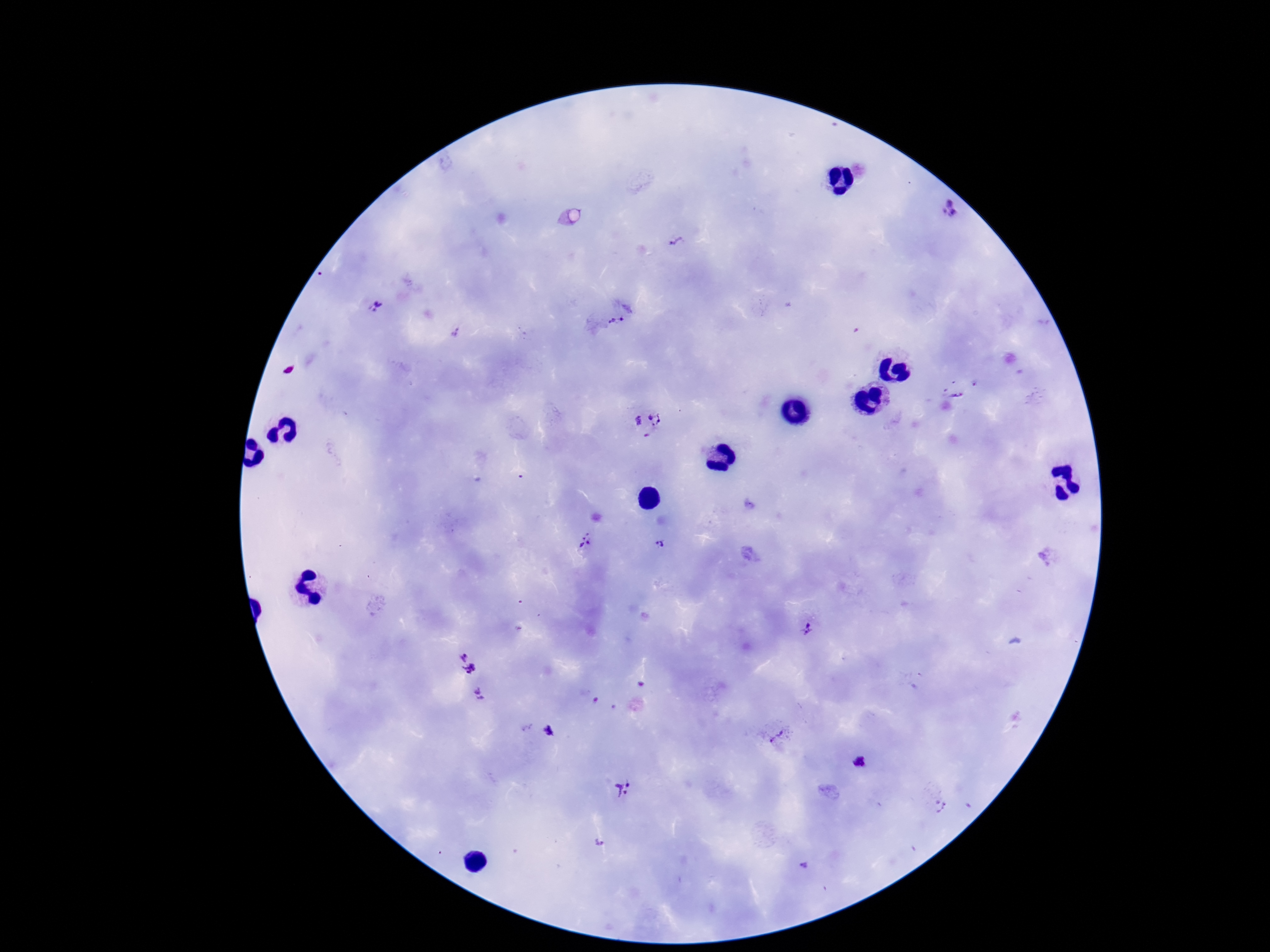
Approximate centers as (x, y) in pixels. Plasmodium parasite locations: (950, 208), (675, 240), (377, 307), (618, 324), (956, 386), (647, 424), (587, 543), (658, 544), (809, 631), (461, 652), (470, 671), (481, 694), (550, 732), (776, 736), (860, 762), (623, 790), (803, 866). Image is 1270×952 pixels. Patient malaria status: positive. Thick blood film. One field from this slide. Smartphone photograph taken through the microscope eyepiece. Giemsa stain. 100x magnification.